Classify this cell by malaria status.
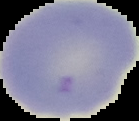
It is uninfected.

Image is 139×121 pixels. From a thin blood smear. Cell region segmented out of the field of view; the surrounding area is masked to black.